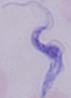

modality = micrograph
magnification = 1000x
identification = trypanosome